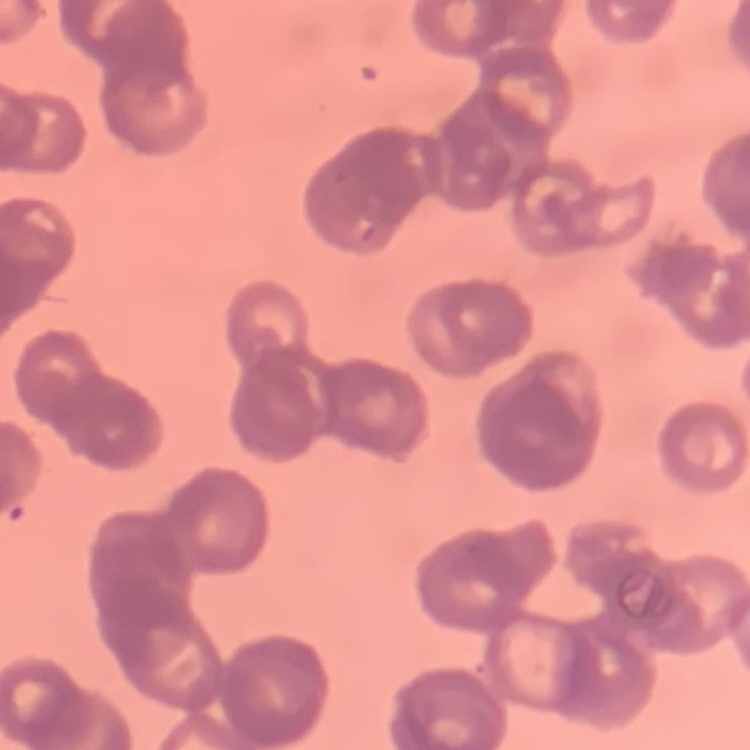
The red blood cells exhibit rouleaux formation. Thin blood smear. Square crop of a larger photomicrograph. Stained with either Field's or Giemsa.